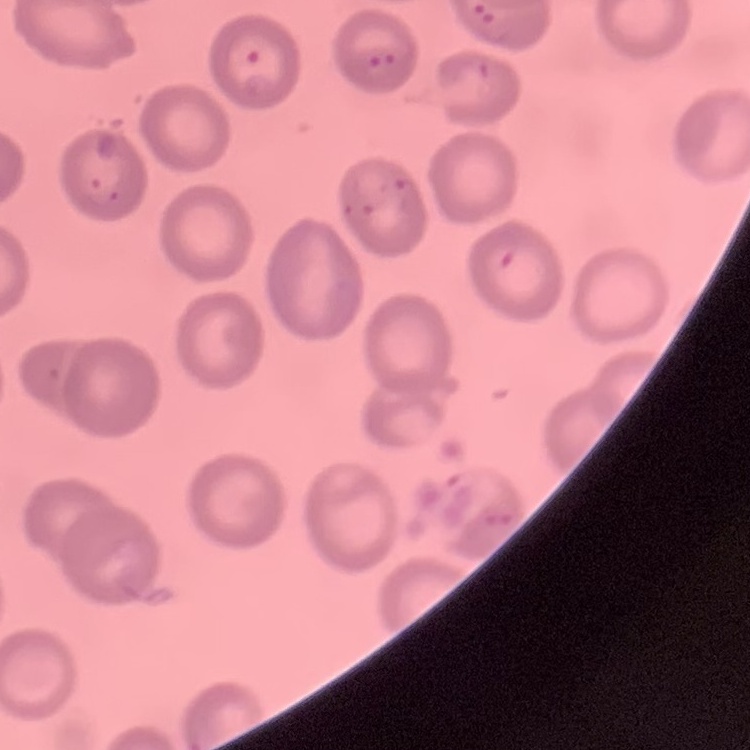
Summary:
  - Erythrocyte morphology: no rouleaux formation
  - Preparation: thin peripheral smear
  - Stain: Field's or Giemsa
  - Image type: square crop of a larger photomicrograph